Point out leukocytes.
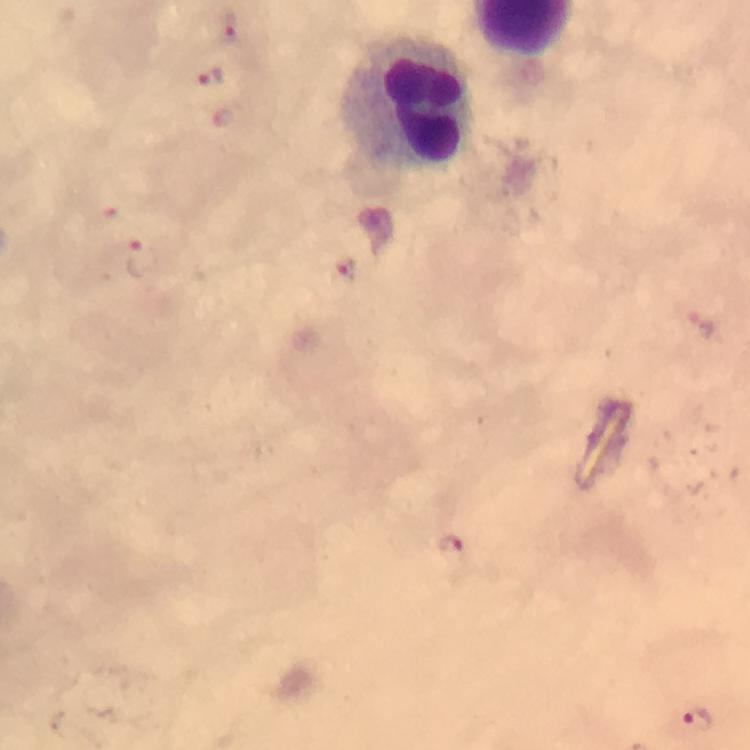
Approximate object centers, in pixels from the top-left corner.
Leukocytes: (x=406, y=101).

immersion_oil: used
preparation: thick blood smear
malaria_parasites: none detected
image_size: 750×750 pixels
context: from a diagnostic examination for malaria
magnification: 100x
cropped_from: one field of view
stain: Giemsa
capture: smartphone mounted on the microscope